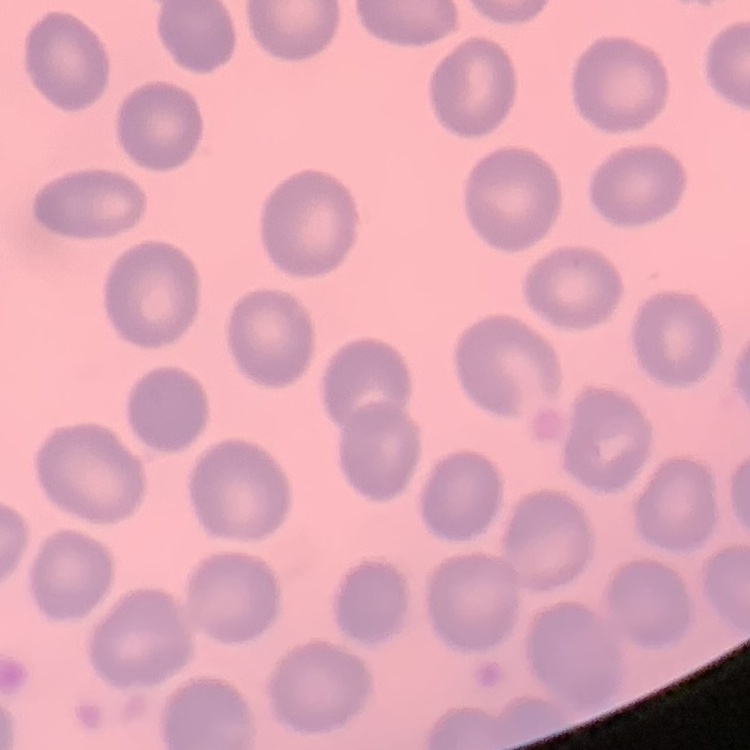 The red blood cells exhibit no rouleaux formation. Stained with either Field's or Giemsa. Thin blood film. Square crop of a larger photomicrograph.